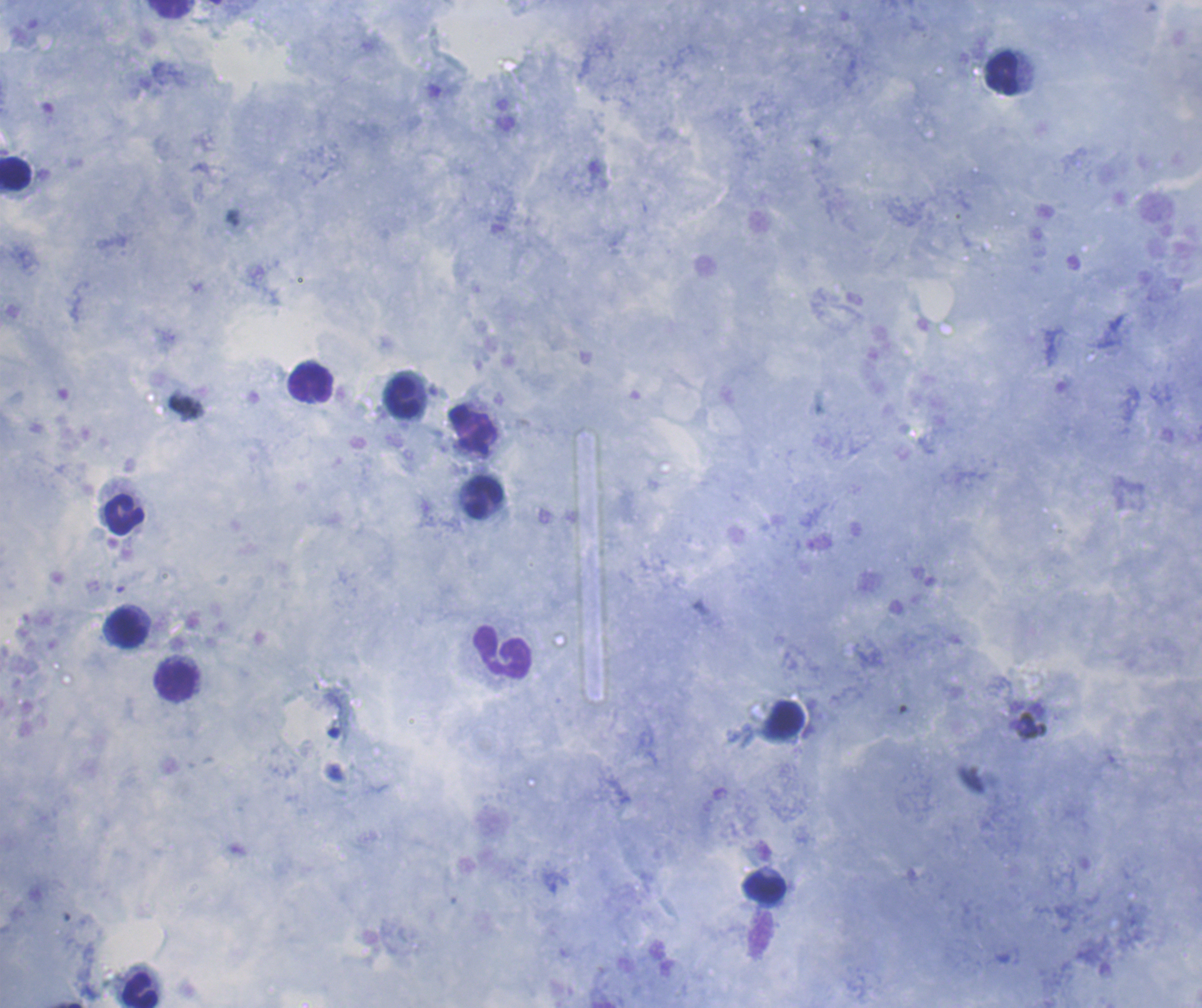
{
  "result": "no Plasmodium parasites detected",
  "field_of_view": "one from this slide",
  "preparation": "thick blood film",
  "coloration_quality": "good",
  "leukocyte_locations": "approximate centers as [x, y] in pixels: [169, 10], [1002, 73], [15, 172], [312, 382], [402, 398], [484, 498], [125, 513], [128, 629], [503, 651], [175, 681], [785, 720], [765, 888], [140, 991]",
  "stain": "Romanowsky",
  "image_size": "1202×1008 pixels",
  "magnification": "100x",
  "background_quality": "good",
  "context": "previously used in a real diagnosis"
}